State which cell type is depicted.
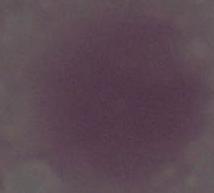

An erythrocyte.

magnification = 1000x
modality = photomicrograph